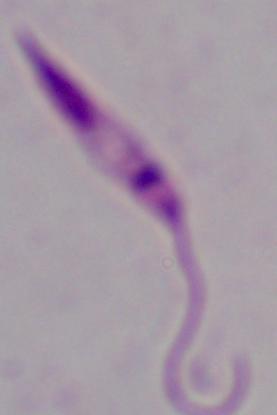
identification = Leishmania
modality = micrograph
magnification = 1000x